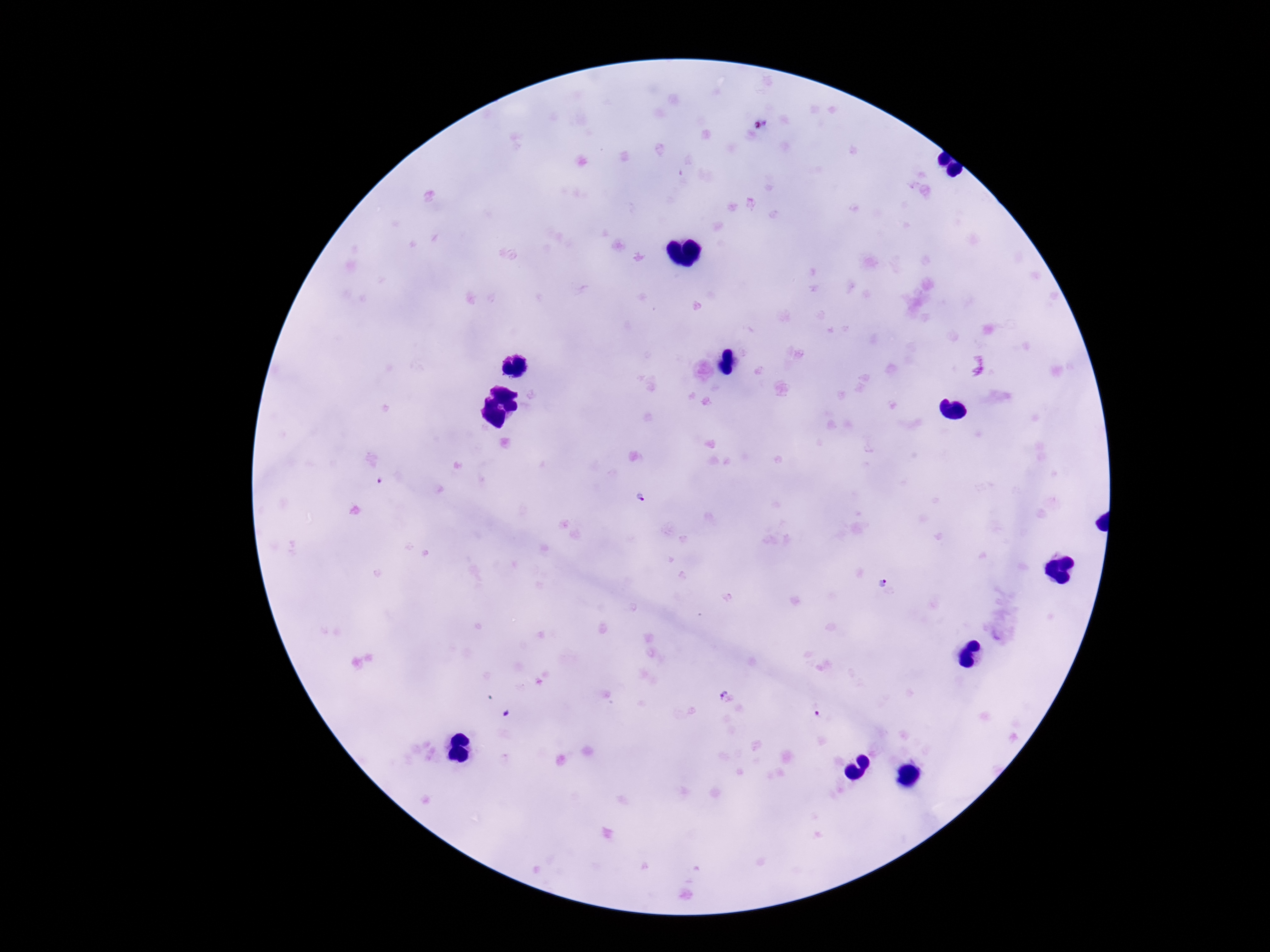

Plasmodium parasite locations = approximate centers as (x, y) in pixels: (765, 120), (643, 500), (883, 585), (724, 695), (820, 715)
image size = 1270×952 pixels
preparation = thick blood smear
capture = smartphone camera through the microscope eyepiece
magnification = 100x
patient malaria status = positive
stain = Giemsa
field of view = one from this slide